Assess this cell for malaria.
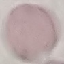
It is uninfected.

Cell patch, automatically extracted from a larger field of view and resized to 64 × 64 pixels. Thin blood film. Photographed with a smartphone camera at the microscope eyepiece. Giemsa stain.